Report the malaria status of this cell.
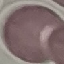
Uninfected.

Summary:
  - Stain: Giemsa
  - Capture: smartphone through the microscope eyepiece
  - Image type: cell patch, automatically extracted from a larger field of view and resized to 64 × 64 pixels
  - Preparation: thin smear